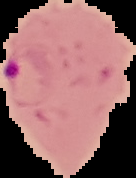 Segmented cell region on a black background. Result: malaria parasites detected. From a thin blood film. Image is 136×178 pixels.